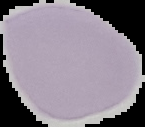 Image is 145×127 pixels. Malaria status: uninfected. Segmented cell region on a black background. From a thin blood film.